Classify this cell by malaria status.
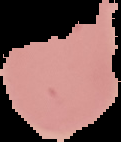
Uninfected.

Summary:
  - Preparation: thin blood smear
  - Image type: segmented cell region with the area outside set to black
  - Image size: 121×142 pixels